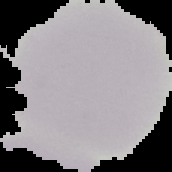

Summary:
  - Preparation: thin blood smear
  - Result: negative for Plasmodium parasites
  - Image size: 172×172 pixels
  - Image type: segmented cell region with the area outside set to black